Give the extent of all white blood cells.
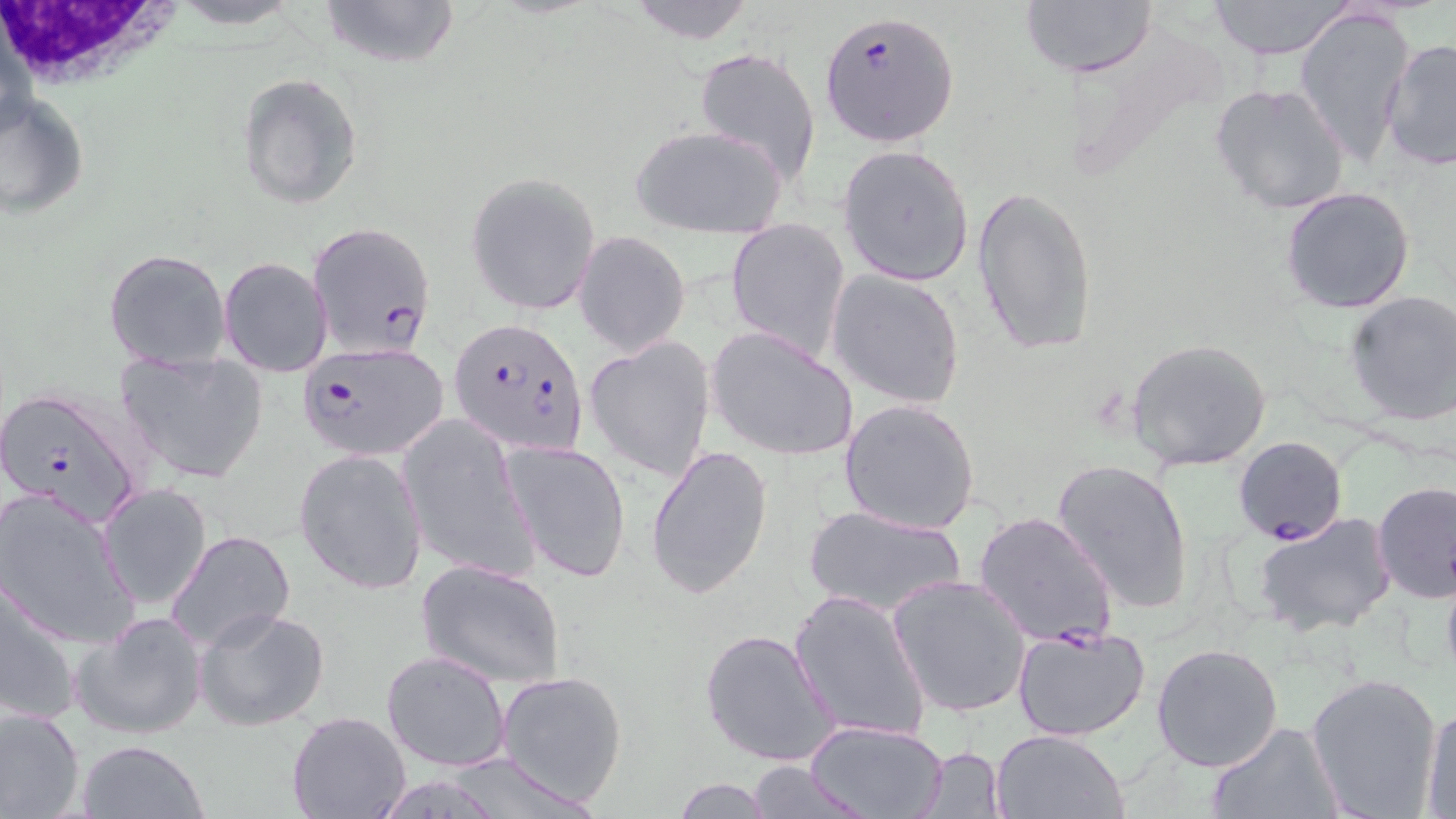

Approximate bounding boxes as [x1, y1, x2, y2] in pixels.
White blood cells: [1, 2, 189, 102].

Uninfected red blood cell locations: [165, 0, 309, 31], [317, 0, 461, 72], [622, 0, 759, 44], [1206, 0, 1359, 59], [1019, 1, 1157, 79], [1293, 6, 1415, 166], [1379, 38, 1455, 172], [694, 48, 822, 186], [237, 73, 363, 210], [1209, 82, 1351, 216], [1, 92, 90, 219], [633, 125, 785, 238], [837, 144, 975, 286], [466, 173, 600, 315], [972, 185, 1097, 359], [1281, 186, 1416, 315], [727, 218, 852, 361], [576, 232, 689, 355], [104, 247, 232, 371], [219, 256, 333, 376], [827, 269, 966, 410], [1343, 291, 1456, 426], [707, 327, 860, 462], [583, 337, 716, 480], [1126, 338, 1273, 472], [114, 351, 268, 483], [839, 398, 981, 536], [397, 415, 539, 583], [500, 440, 633, 583], [647, 442, 773, 599], [294, 449, 428, 595], [1052, 457, 1196, 614], [99, 481, 212, 609], [1373, 482, 1455, 604], [1, 487, 141, 647], [801, 504, 967, 618], [1253, 512, 1397, 637], [165, 529, 295, 654], [416, 559, 566, 688], [888, 574, 1032, 718], [2, 578, 84, 726], [790, 589, 931, 744], [194, 605, 331, 732], [72, 611, 209, 741], [1013, 625, 1151, 742], [699, 627, 839, 767], [1151, 642, 1284, 772], [380, 650, 512, 771], [496, 670, 628, 806], [1306, 671, 1444, 816], [1420, 703, 1456, 816], [0, 705, 85, 819], [287, 711, 412, 819], [805, 720, 951, 819], [1204, 721, 1342, 819], [991, 728, 1128, 818], [75, 739, 208, 819], [916, 745, 1008, 817], [743, 761, 876, 816], [670, 778, 776, 817]. Plasmodium falciparum-infected red blood cell locations: [822, 10, 957, 145], [306, 220, 437, 360], [449, 316, 590, 458], [295, 342, 450, 463], [0, 385, 151, 528], [1233, 435, 1347, 546], [973, 510, 1119, 649]. Slide-level diagnosis: Plasmodium falciparum. May-Grünwald-Giemsa-stained preparation. Optical microscopy. Image is 1456×819 pixels. One field of a larger specimen. Thin blood smear. 1000x magnification.